Locate every Plasmodium falciparum parasite and give its life-cycle stage, and locate every leukocyte and any debris.
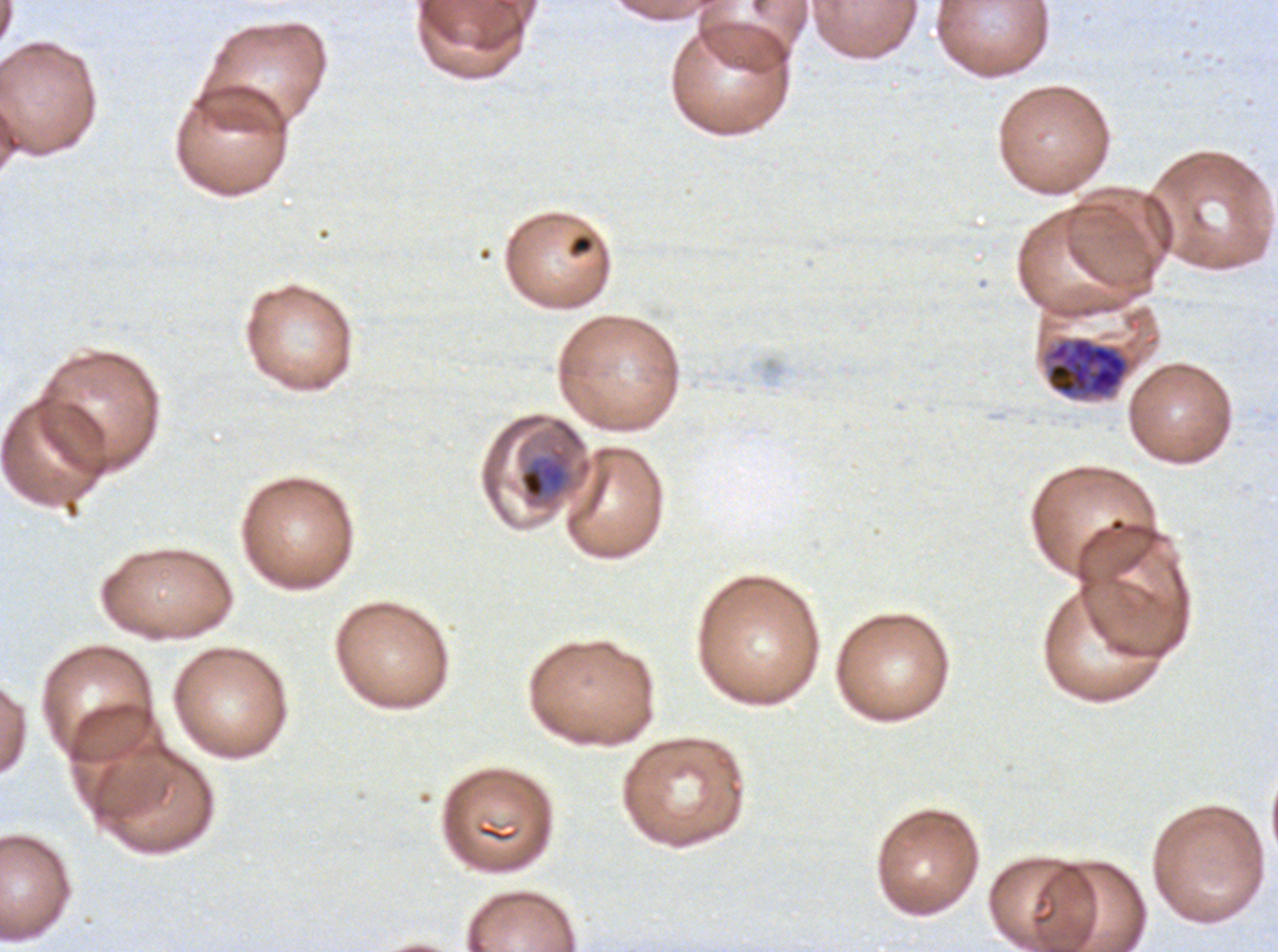

Approximate bounding boxes as [x1, y1, x2, y2] in pixels.
Mid trophozoites: [520, 459, 566, 500].
Late trophozoites: [1045, 336, 1129, 398].
Debris: [568, 234, 595, 257].
No rings, late-ring/early-trophozoite forms, early schizonts, late schizonts, segmenters, gametocytes, or leukocytes observed.

field of view = one sub-image of a larger composite
life-cycle stages observed = mid trophozoite, late trophozoite
image size = 1278×952 pixels
specimen = Plasmodium falciparum from a patient in The Gambia, cultured ex vivo for 24 to 48 hours
preparation = thin blood film
stain = Giemsa